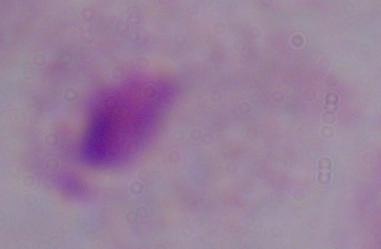

Summary:
  - Magnification: 1000x
  - Modality: micrograph
  - Identification: trichomonad